Outline each blood parasite and name the species.
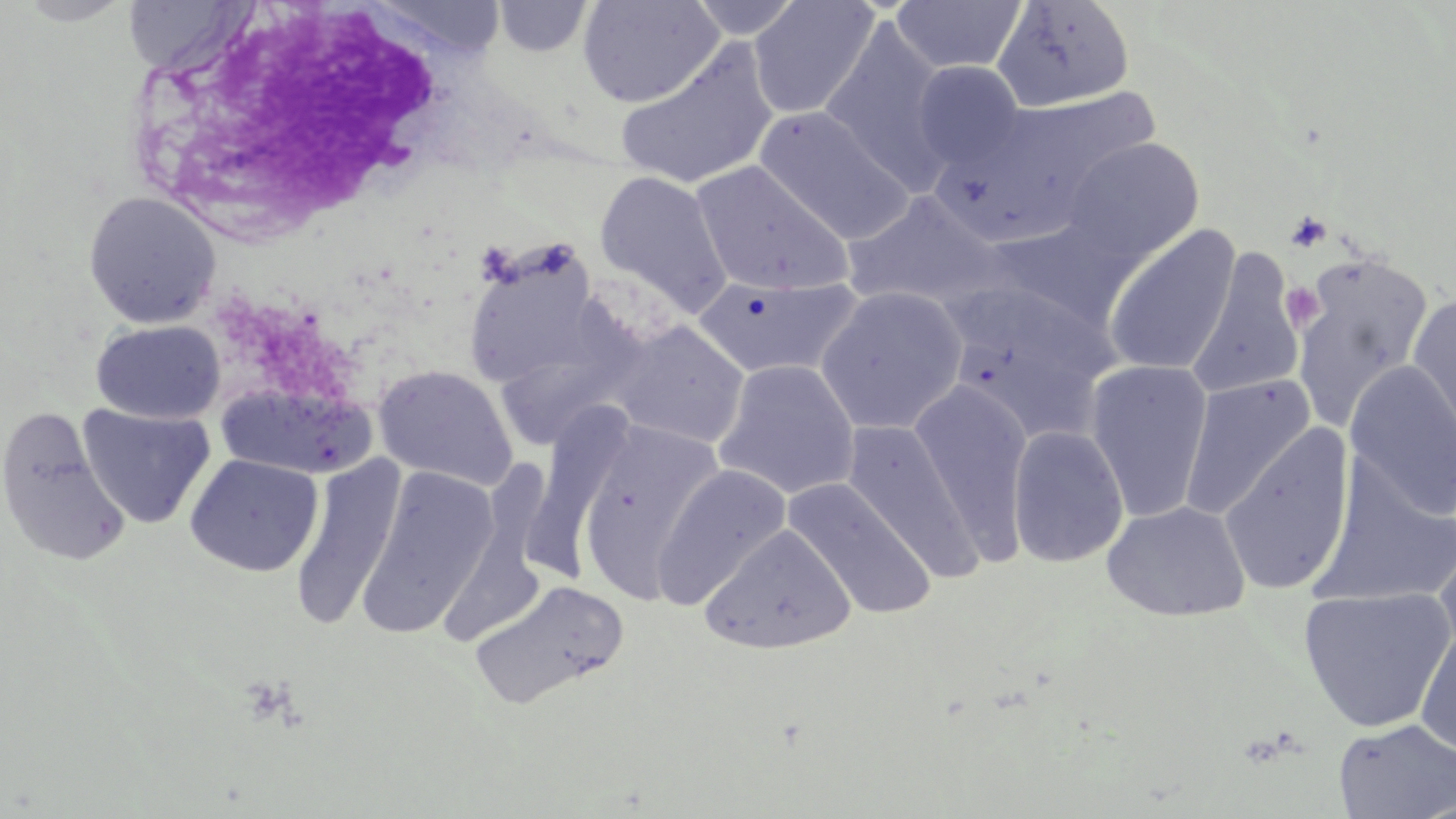

No blood parasites seen.

Approximate bounding boxes as named x1/y1/x2/y2 corners in pixels. White blood cell locations: (x1=130, y1=0, x2=463, y2=240). Platelet locations: (x1=1286, y1=211, x2=1332, y2=253), (x1=1280, y1=282, x2=1325, y2=331), (x1=237, y1=675, x2=302, y2=731). Uninfected red blood cell locations: (x1=11, y1=0, x2=137, y2=26), (x1=370, y1=0, x2=506, y2=61), (x1=577, y1=0, x2=724, y2=108), (x1=687, y1=0, x2=804, y2=39), (x1=749, y1=0, x2=879, y2=119), (x1=890, y1=0, x2=1025, y2=75), (x1=493, y1=1, x2=593, y2=58), (x1=992, y1=1, x2=1135, y2=112), (x1=819, y1=20, x2=953, y2=191), (x1=617, y1=42, x2=780, y2=191), (x1=912, y1=60, x2=1026, y2=170), (x1=973, y1=88, x2=1165, y2=220), (x1=755, y1=106, x2=914, y2=244), (x1=1062, y1=137, x2=1205, y2=264), (x1=690, y1=160, x2=854, y2=298), (x1=595, y1=170, x2=732, y2=315), (x1=82, y1=191, x2=222, y2=329), (x1=842, y1=192, x2=1004, y2=309), (x1=1104, y1=225, x2=1240, y2=377), (x1=466, y1=240, x2=590, y2=386), (x1=1187, y1=252, x2=1305, y2=400), (x1=1291, y1=253, x2=1434, y2=431), (x1=693, y1=274, x2=862, y2=380), (x1=942, y1=283, x2=1120, y2=441), (x1=815, y1=285, x2=968, y2=436), (x1=1407, y1=292, x2=1456, y2=453), (x1=511, y1=301, x2=645, y2=449), (x1=91, y1=320, x2=225, y2=424), (x1=610, y1=321, x2=750, y2=449), (x1=714, y1=359, x2=860, y2=501), (x1=1085, y1=359, x2=1214, y2=521), (x1=1344, y1=361, x2=1456, y2=521), (x1=373, y1=364, x2=519, y2=491), (x1=1180, y1=375, x2=1314, y2=520), (x1=910, y1=380, x2=1033, y2=563), (x1=220, y1=381, x2=377, y2=480), (x1=531, y1=403, x2=640, y2=588), (x1=78, y1=404, x2=216, y2=529), (x1=0, y1=406, x2=131, y2=567), (x1=842, y1=419, x2=984, y2=582), (x1=577, y1=421, x2=725, y2=599), (x1=1217, y1=423, x2=1355, y2=597), (x1=1007, y1=424, x2=1129, y2=568), (x1=184, y1=454, x2=323, y2=577), (x1=290, y1=456, x2=405, y2=631), (x1=453, y1=457, x2=554, y2=641), (x1=652, y1=463, x2=792, y2=607), (x1=357, y1=466, x2=499, y2=637), (x1=784, y1=477, x2=936, y2=620), (x1=1102, y1=500, x2=1251, y2=622), (x1=700, y1=523, x2=856, y2=654), (x1=1431, y1=539, x2=1456, y2=670), (x1=468, y1=579, x2=629, y2=711), (x1=1298, y1=587, x2=1455, y2=732), (x1=1415, y1=622, x2=1456, y2=759), (x1=1333, y1=718, x2=1456, y2=818). Slide-level diagnosis: no evidence of blood parasites. May-Grünwald-Giemsa stain. Captured at 1000x magnification. Single field of view. Image is 1456×819 pixels. Light microscopy. Thin blood smear.